Assess the morphology of the red blood cells.
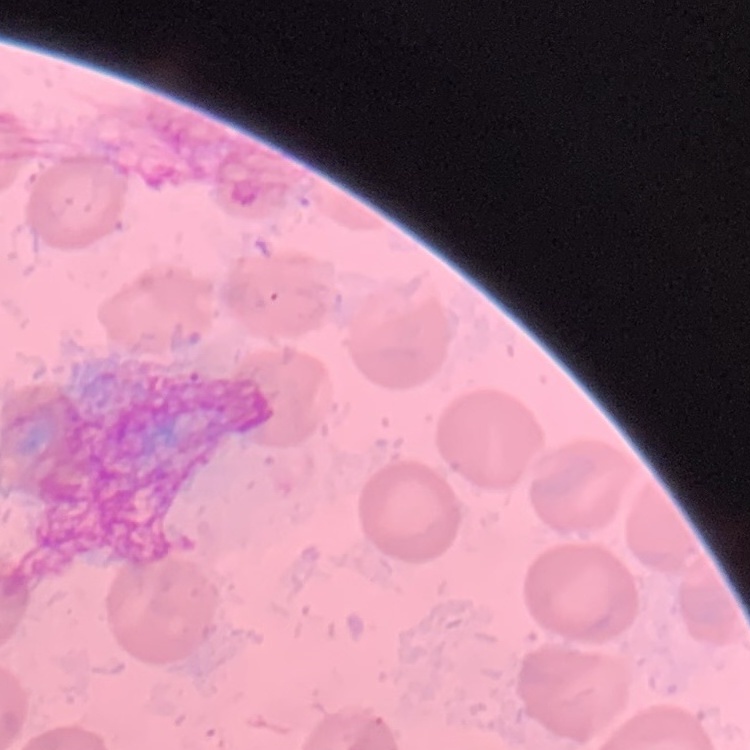
They show no rouleaux formation.

Summary:
  - Stain: Field's or Giemsa
  - Preparation: thin peripheral smear
  - Image type: one tile cut from a larger photomicrograph